Identify the parasite.
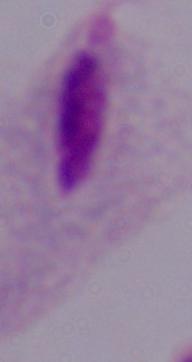

A trichomonad.

Summary:
  - Magnification: 1000x
  - Modality: micrograph